Name the cell type shown.
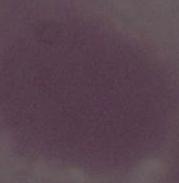

This is an erythrocyte.

Summary:
  - Modality: photomicrograph
  - Magnification: 1000x